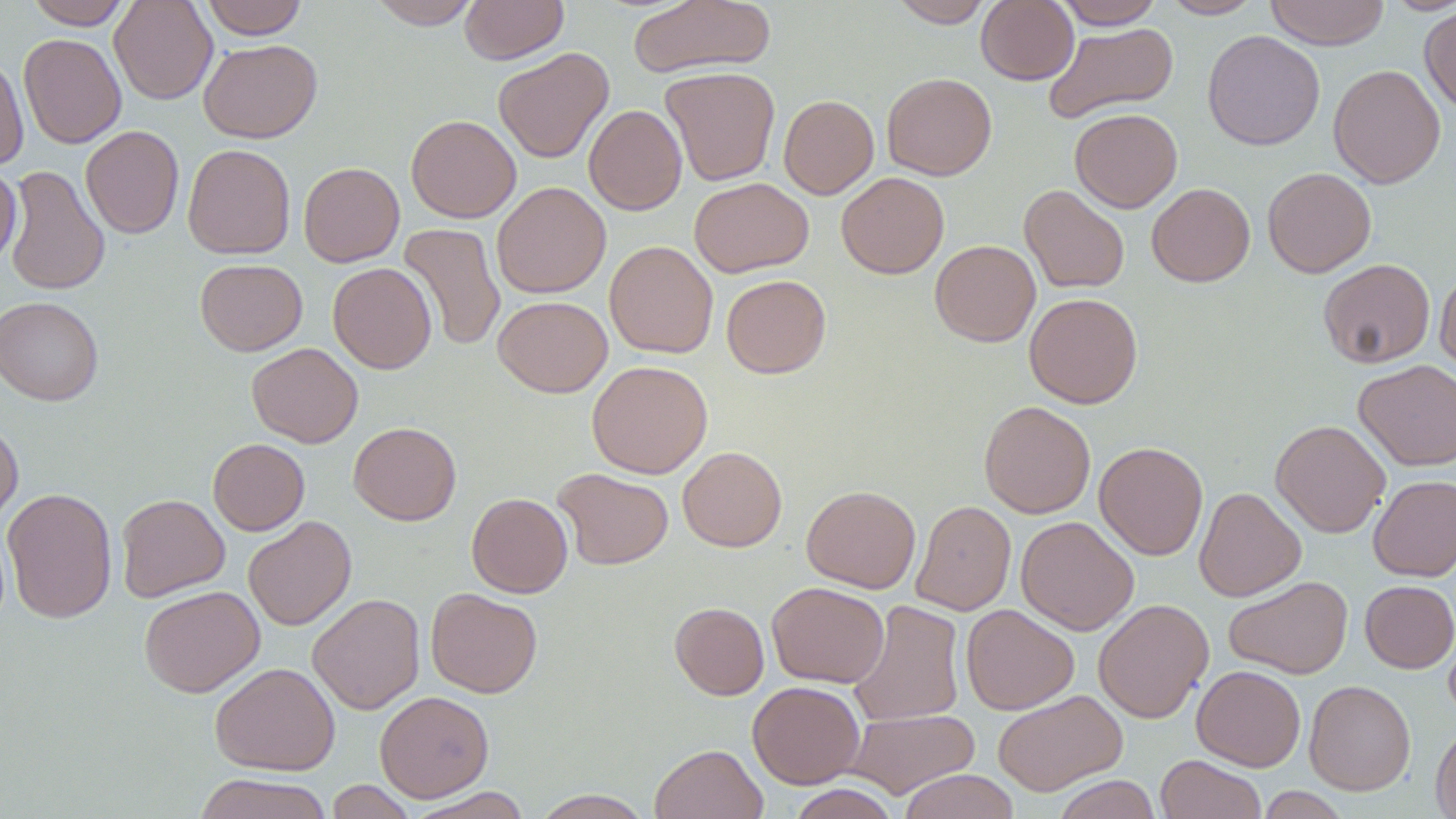

Approximate bounding boxes as [x1, y1, x2, y2] in pixels. Uninfected red blood cell locations: [24, 0, 134, 29], [109, 0, 217, 105], [199, 0, 309, 39], [366, 0, 484, 29], [459, 0, 568, 64], [628, 0, 776, 80], [889, 0, 995, 27], [976, 0, 1078, 85], [1052, 0, 1164, 29], [1159, 0, 1264, 19], [1264, 0, 1390, 49], [1383, 0, 1456, 15], [1419, 6, 1456, 117], [1044, 22, 1179, 124], [1202, 30, 1326, 151], [18, 33, 126, 149], [198, 38, 322, 143], [493, 47, 614, 163], [0, 54, 30, 172], [1328, 63, 1446, 188], [660, 66, 780, 186], [881, 72, 997, 180], [778, 94, 879, 199], [584, 105, 687, 215], [1069, 108, 1182, 212], [406, 114, 521, 223], [80, 125, 184, 239], [183, 143, 296, 259], [298, 161, 404, 267], [0, 164, 22, 270], [4, 165, 110, 296], [1262, 167, 1376, 278], [836, 172, 949, 279], [689, 177, 814, 278], [491, 181, 611, 298], [1146, 183, 1255, 286], [1019, 185, 1130, 294], [399, 222, 506, 352], [930, 239, 1040, 347], [604, 240, 718, 358], [1318, 258, 1435, 368], [195, 259, 307, 356], [328, 262, 436, 374], [1435, 265, 1456, 380], [721, 274, 831, 378], [1024, 292, 1143, 408], [493, 295, 612, 397], [0, 296, 104, 406], [246, 343, 363, 448], [1353, 359, 1456, 471], [587, 360, 713, 479], [978, 400, 1096, 518], [0, 418, 23, 526], [1271, 419, 1390, 537], [349, 422, 461, 525], [208, 438, 309, 535], [1094, 441, 1208, 560], [678, 446, 787, 552], [552, 468, 674, 570], [1368, 475, 1456, 582], [801, 485, 921, 593], [1194, 486, 1306, 602], [2, 487, 118, 624], [466, 493, 572, 598], [116, 494, 229, 601], [911, 500, 1016, 615], [243, 516, 356, 631], [1016, 516, 1139, 635], [1223, 575, 1352, 679], [1360, 580, 1456, 673], [767, 582, 889, 688], [138, 585, 265, 698], [426, 588, 542, 698], [307, 593, 425, 715], [1093, 598, 1213, 723], [848, 600, 965, 727], [670, 602, 769, 700], [961, 604, 1080, 715], [210, 661, 340, 775], [1192, 665, 1305, 771], [1304, 679, 1415, 796], [747, 681, 865, 788], [992, 689, 1127, 796], [374, 690, 494, 802], [846, 708, 980, 798], [1430, 722, 1456, 819], [649, 743, 768, 819], [1155, 754, 1267, 819], [899, 769, 1019, 819], [193, 772, 334, 819], [1052, 775, 1162, 819], [325, 780, 416, 819], [787, 784, 900, 819], [407, 787, 532, 818], [1255, 788, 1350, 818], [530, 789, 654, 818]. Slide-level diagnosis: no evidence of blood parasites. 1000x magnification. Thin blood smear. Optical microscopy. One field of a larger specimen. May-Grünwald-Giemsa-stained preparation. Image is 1456×819 pixels.